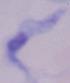
magnification: 1000x
modality: photomicrograph
identification: trypanosome